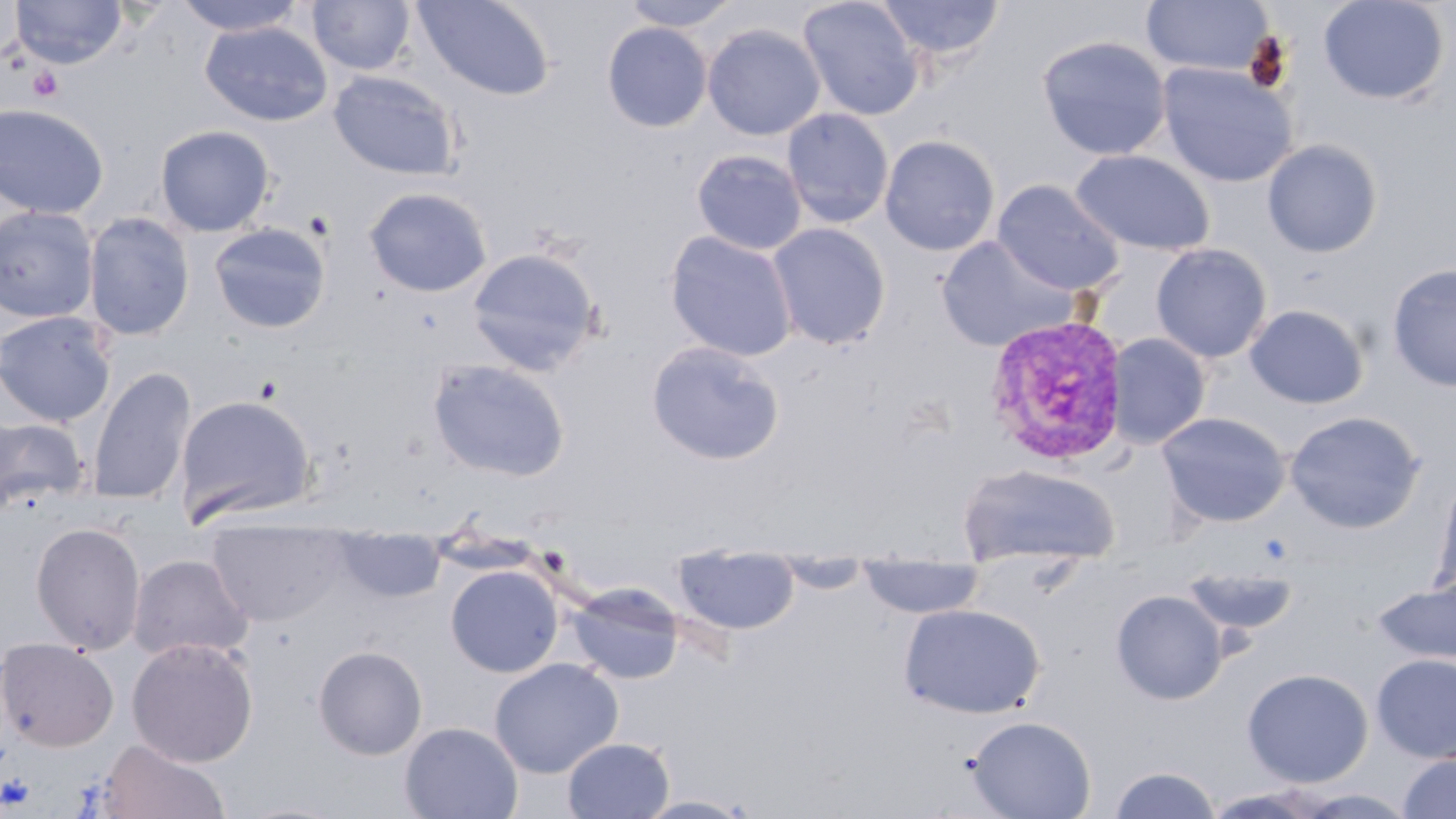

Summary:
  - Coordinate format: approximate bounding boxes as (x1, y1, x2, y2) in pixels
  - Uninfected red blood cell locations: (10, 0, 127, 69), (172, 0, 308, 37), (308, 0, 415, 76), (413, 0, 556, 101), (619, 0, 744, 31), (797, 0, 925, 121), (873, 0, 1006, 65), (1318, 0, 1450, 105), (1141, 1, 1275, 77), (200, 21, 333, 126), (602, 22, 713, 133), (702, 23, 825, 141), (1037, 35, 1172, 161), (1157, 62, 1298, 188), (328, 70, 462, 180), (0, 102, 110, 219), (781, 107, 894, 229), (155, 125, 275, 236), (879, 134, 1000, 256), (1262, 139, 1383, 258), (692, 150, 807, 255), (1071, 150, 1214, 256), (992, 180, 1125, 296), (364, 187, 492, 298), (0, 206, 100, 323), (84, 213, 196, 342), (207, 222, 332, 335), (768, 223, 891, 349), (665, 231, 797, 362), (936, 236, 1079, 352), (1150, 243, 1272, 363), (465, 246, 603, 376), (1386, 263, 1456, 392), (1244, 304, 1369, 409), (0, 311, 116, 427), (1106, 333, 1211, 448), (646, 341, 785, 466), (427, 358, 571, 482), (86, 366, 196, 506), (175, 393, 318, 527), (1284, 410, 1425, 533), (1157, 411, 1291, 527), (0, 416, 90, 514), (957, 464, 1120, 567), (1431, 475, 1456, 601), (207, 518, 348, 626), (30, 521, 146, 654), (334, 532, 445, 603), (128, 553, 253, 663), (673, 554, 800, 634), (772, 559, 873, 592), (857, 562, 986, 619), (1180, 564, 1299, 639), (445, 565, 563, 677), (1373, 578, 1456, 665), (568, 583, 685, 685), (1111, 590, 1228, 704), (898, 603, 1046, 719), (0, 638, 119, 752), (126, 638, 259, 767), (313, 645, 427, 760), (1372, 654, 1456, 763), (489, 658, 623, 778), (1241, 667, 1374, 788), (967, 715, 1096, 819), (399, 722, 523, 818), (561, 737, 675, 818), (95, 739, 230, 819), (1397, 752, 1456, 819), (1107, 765, 1223, 818), (635, 794, 757, 819)
  - Platelet locations: (28, 67, 63, 102)
  - Plasmodium vivax-infected red blood cell locations: (984, 314, 1131, 467)
  - Slide-level diagnosis: Plasmodium vivax
  - Modality: optical microscopy
  - Magnification: 1000x
  - Image size: 1456×819 pixels
  - Field of view: one of a larger specimen
  - Stain: May-Grünwald-Giemsa
  - Preparation: thin blood smear